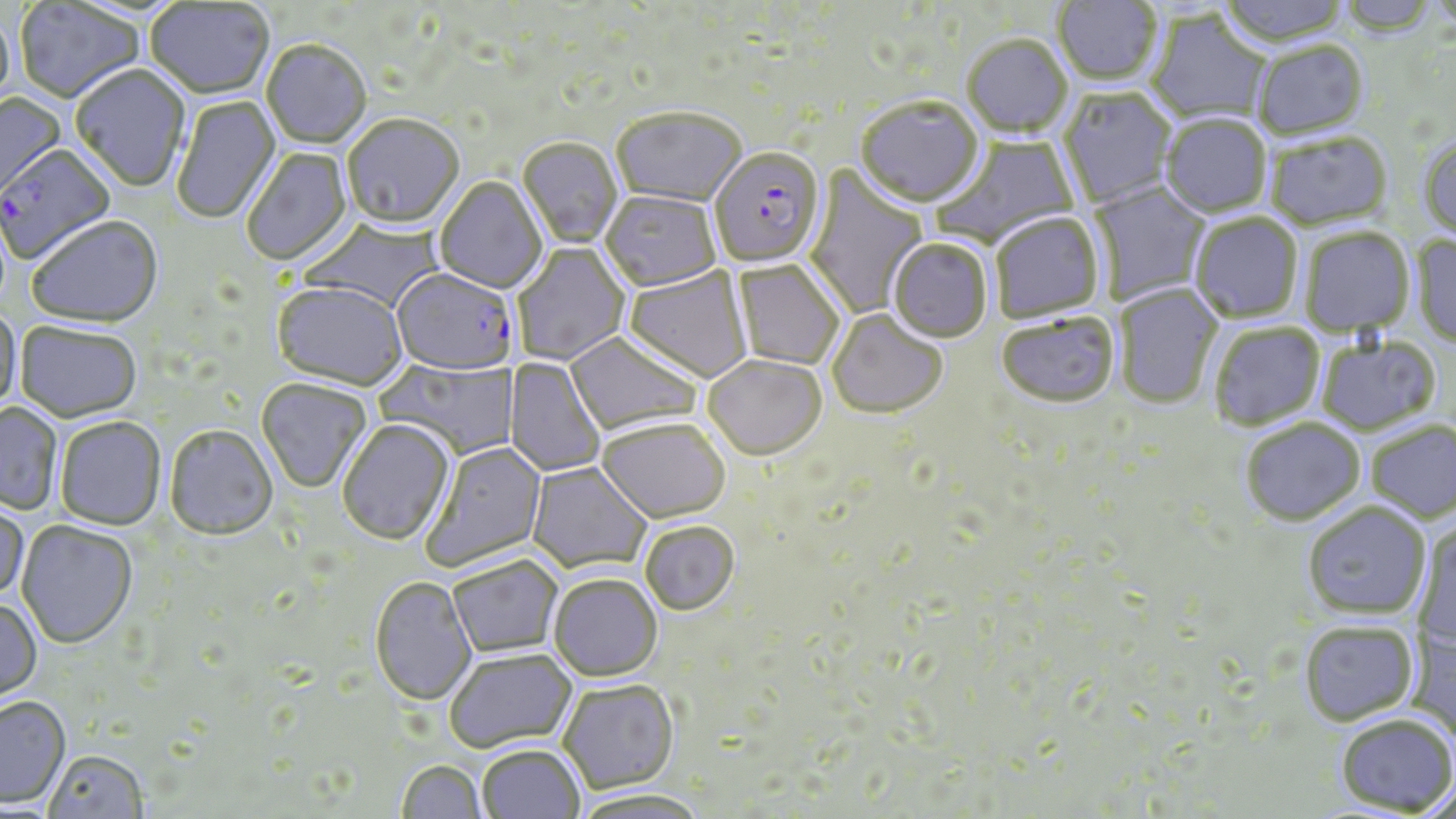 Approximate bounding boxes as [x1, y1, x2, y2] in pixels. Uninfected red blood cell locations: [1051, 0, 1163, 88], [1216, 0, 1351, 50], [1337, 0, 1440, 39], [13, 2, 146, 106], [146, 2, 275, 100], [0, 10, 16, 119], [1145, 11, 1273, 126], [962, 38, 1073, 140], [261, 42, 371, 150], [1252, 43, 1370, 143], [70, 66, 190, 193], [1058, 88, 1177, 208], [0, 93, 67, 206], [172, 96, 281, 225], [854, 99, 985, 210], [610, 111, 748, 210], [1160, 116, 1272, 219], [342, 117, 465, 231], [931, 133, 1082, 252], [1264, 135, 1393, 233], [1418, 136, 1456, 247], [518, 139, 623, 249], [242, 147, 353, 267], [804, 163, 929, 320], [435, 178, 548, 295], [1086, 181, 1211, 306], [600, 192, 722, 294], [990, 213, 1105, 325], [1189, 213, 1303, 325], [26, 218, 164, 330], [1300, 228, 1415, 337], [1410, 234, 1456, 350], [887, 240, 993, 345], [512, 243, 630, 365], [730, 260, 845, 371], [624, 266, 753, 384], [271, 283, 409, 393], [1114, 283, 1224, 410], [0, 308, 22, 416], [827, 310, 948, 420], [996, 316, 1119, 410], [15, 323, 142, 426], [1209, 323, 1325, 431], [564, 332, 704, 438], [1316, 337, 1441, 436], [376, 357, 518, 460], [504, 357, 606, 477], [703, 357, 826, 464], [256, 379, 372, 493], [0, 403, 62, 515], [55, 418, 167, 531], [1240, 418, 1365, 525], [337, 420, 455, 547], [1366, 420, 1456, 522], [596, 421, 730, 525], [164, 427, 279, 543], [420, 440, 548, 572], [527, 462, 652, 575], [0, 498, 29, 602], [1302, 502, 1431, 619], [1411, 519, 1455, 649], [16, 521, 138, 650], [640, 523, 740, 617], [448, 556, 563, 658], [549, 574, 663, 683], [370, 578, 477, 708], [0, 599, 43, 704], [1298, 620, 1419, 726], [445, 651, 578, 754], [558, 681, 680, 795], [0, 698, 71, 809], [1335, 713, 1456, 815], [477, 745, 584, 819], [44, 752, 149, 819], [396, 761, 486, 819], [571, 792, 711, 819]. Plasmodium falciparum-infected red blood cell locations: [0, 146, 117, 266], [709, 149, 826, 269], [390, 271, 516, 375]. Slide-level diagnosis: Plasmodium falciparum. Optical microscopy. May-Grünwald-Giemsa-stained preparation. Thin blood smear. Image is 1456×819 pixels. Captured at 1000x magnification. One field of a larger specimen.